Identify the parasite.
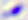

Toxoplasma gondii.

Captured at 400x magnification. Photomicrograph.